Describe the morphology of the erythrocytes.
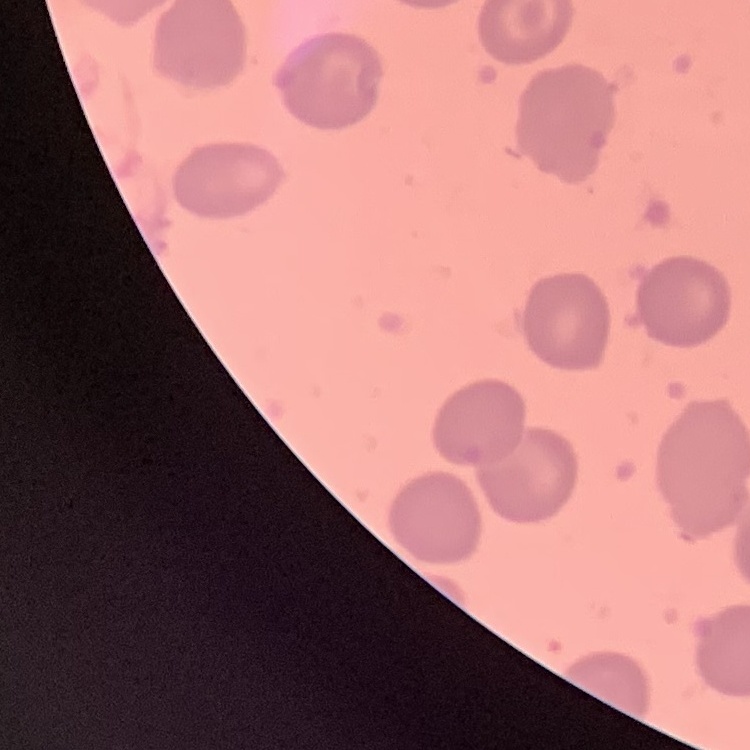

They show no rouleaux formation.

Summary:
  - Image type: one tile cut from a larger photomicrograph
  - Preparation: thin blood smear
  - Stain: Field's or Giemsa